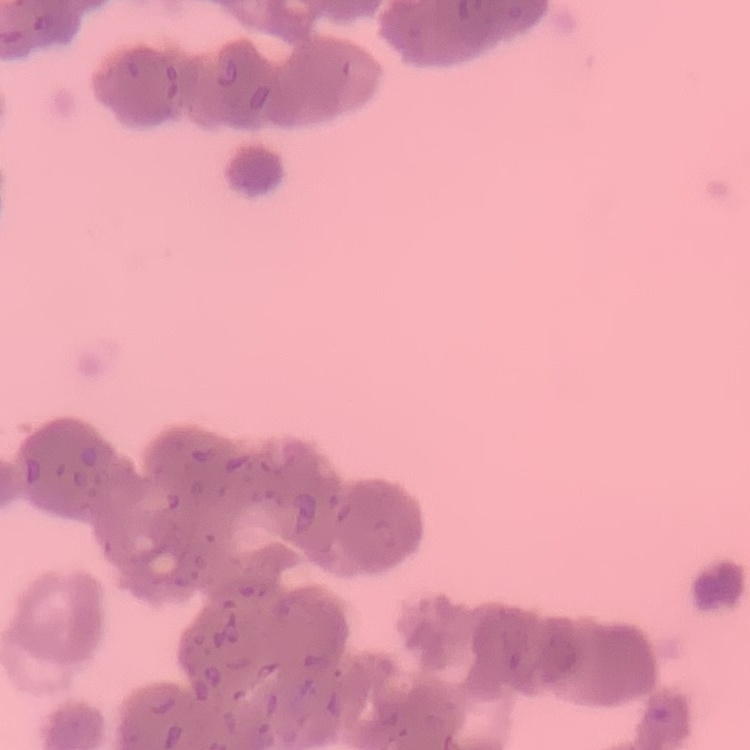

red blood cell morphology = rouleaux formation
stain = Field's or Giemsa
preparation = thin peripheral smear
image type = square crop of a larger photomicrograph